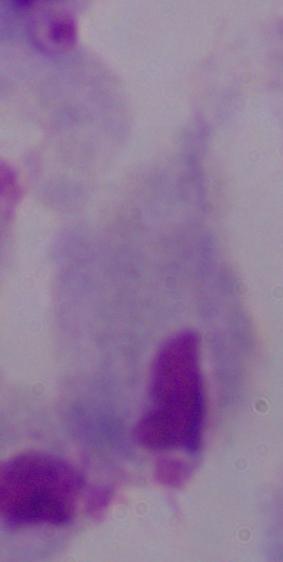
{
  "modality": "photomicrograph",
  "magnification": "1000x",
  "identification": "trichomonad"
}